Assess this cell for malaria.
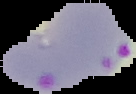

It is parasitized.

The area outside the segmented cell region is set to black. Image is 136×94 pixels. From a thin blood smear.